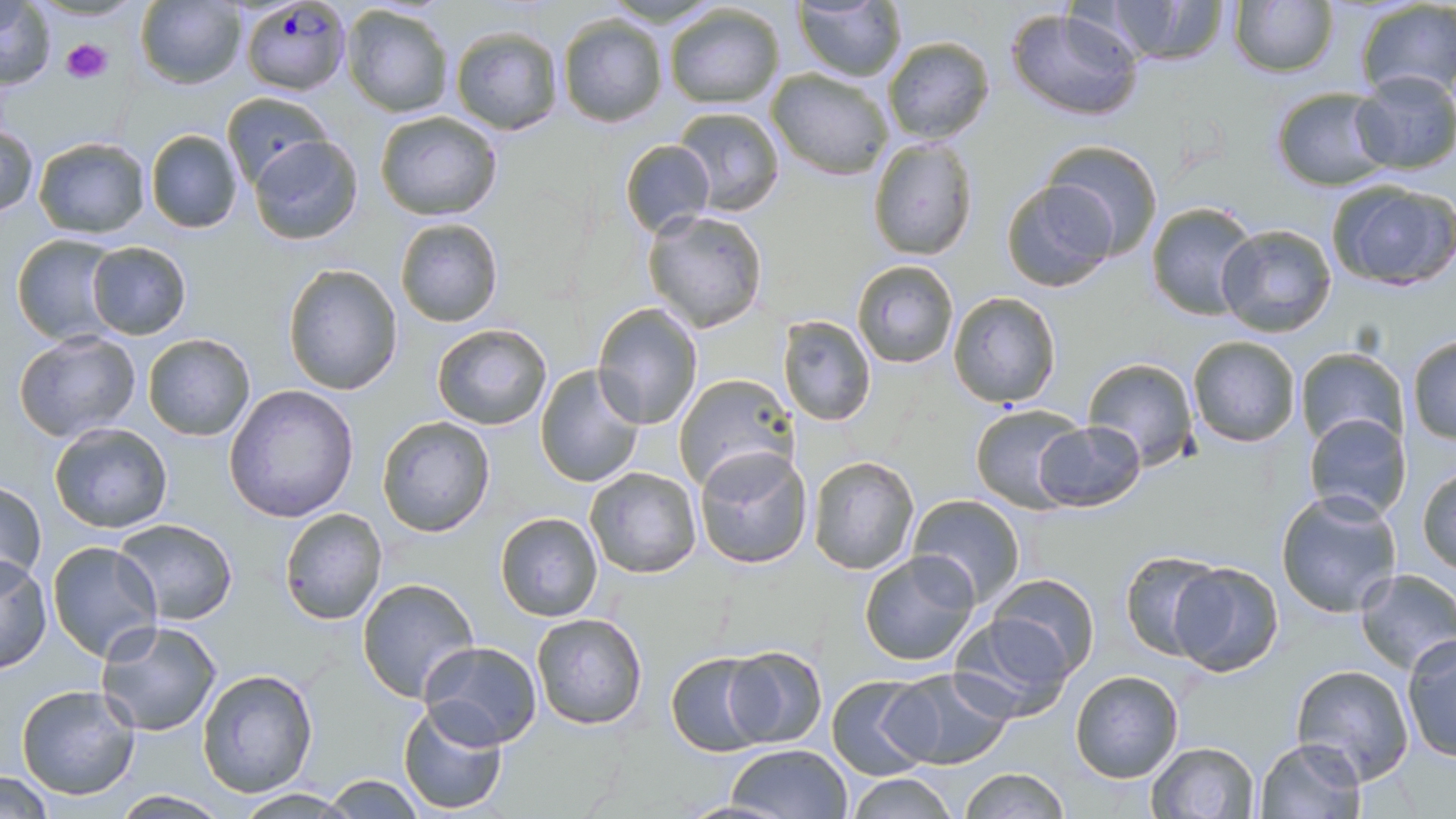

Approximate bounding boxes as (x1, y1, x2, y2) in pixels. Plasmodium falciparum-infected red blood cell locations: (238, 2, 350, 99). Uninfected red blood cell locations: (1098, 0, 1231, 66), (0, 1, 57, 89), (135, 1, 248, 90), (1228, 1, 1337, 77), (1354, 1, 1456, 99), (792, 2, 906, 81), (340, 4, 455, 118), (662, 4, 785, 109), (1007, 7, 1144, 122), (557, 15, 668, 127), (449, 25, 565, 136), (881, 35, 995, 144), (49, 36, 115, 85), (767, 69, 895, 179), (1350, 71, 1456, 173), (1270, 86, 1394, 191), (220, 91, 333, 190), (672, 105, 784, 217), (374, 110, 504, 222), (1, 121, 39, 219), (144, 128, 244, 234), (249, 135, 362, 244), (30, 137, 152, 239), (868, 137, 976, 261), (620, 139, 715, 237), (1043, 139, 1163, 259), (1000, 179, 1121, 293), (1325, 180, 1456, 290), (1145, 199, 1260, 321), (642, 208, 768, 332), (394, 217, 503, 326), (1215, 223, 1338, 336), (11, 234, 122, 345), (84, 241, 192, 339), (851, 259, 958, 368), (283, 262, 403, 395), (949, 292, 1061, 408), (592, 302, 704, 430), (779, 314, 876, 427), (431, 323, 552, 431), (12, 331, 143, 446), (142, 333, 257, 441), (1407, 334, 1456, 445), (1187, 336, 1301, 449), (1294, 347, 1408, 451), (1082, 357, 1198, 470), (535, 365, 645, 486), (673, 371, 795, 495), (224, 384, 359, 523), (970, 402, 1086, 511), (1302, 412, 1411, 522), (374, 415, 496, 538), (1034, 420, 1145, 511), (48, 421, 174, 533), (695, 447, 811, 569), (808, 455, 921, 574), (585, 466, 702, 578), (1417, 468, 1456, 577), (0, 480, 44, 587), (1275, 489, 1403, 617), (907, 494, 1028, 608), (278, 507, 389, 625), (494, 511, 603, 623), (110, 518, 238, 624), (45, 539, 163, 664), (1120, 548, 1223, 658), (858, 550, 981, 665), (0, 556, 52, 674), (1169, 561, 1285, 677), (1354, 567, 1456, 675), (988, 572, 1100, 679), (355, 577, 480, 701), (530, 611, 649, 730), (949, 612, 1076, 723), (94, 620, 223, 737), (1401, 633, 1456, 762), (418, 640, 543, 750), (722, 647, 827, 748), (665, 651, 773, 759), (1290, 664, 1416, 784), (197, 667, 320, 797), (885, 667, 1015, 770), (1068, 670, 1183, 783), (826, 675, 935, 779), (16, 682, 142, 801), (397, 701, 509, 816), (1253, 738, 1366, 819), (1145, 741, 1261, 819), (727, 743, 851, 819), (957, 766, 1069, 819), (0, 771, 56, 815), (321, 773, 425, 817), (846, 773, 957, 819), (230, 788, 361, 817), (111, 789, 228, 818). Platelet locations: (60, 38, 112, 84). Slide-level diagnosis: Plasmodium falciparum. Thin blood film. Optical microscopy. Image is 1456×819 pixels. Captured at 1000x magnification. One field of a larger specimen. May-Grünwald-Giemsa-stained preparation.